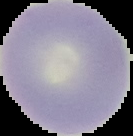

image type = segmented cell region on a black background
image size = 133×136 pixels
result = no Plasmodium parasites detected
preparation = thin blood film